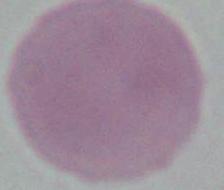

Summary:
  - Identification: red blood cell
  - Modality: photomicrograph
  - Magnification: 1000x